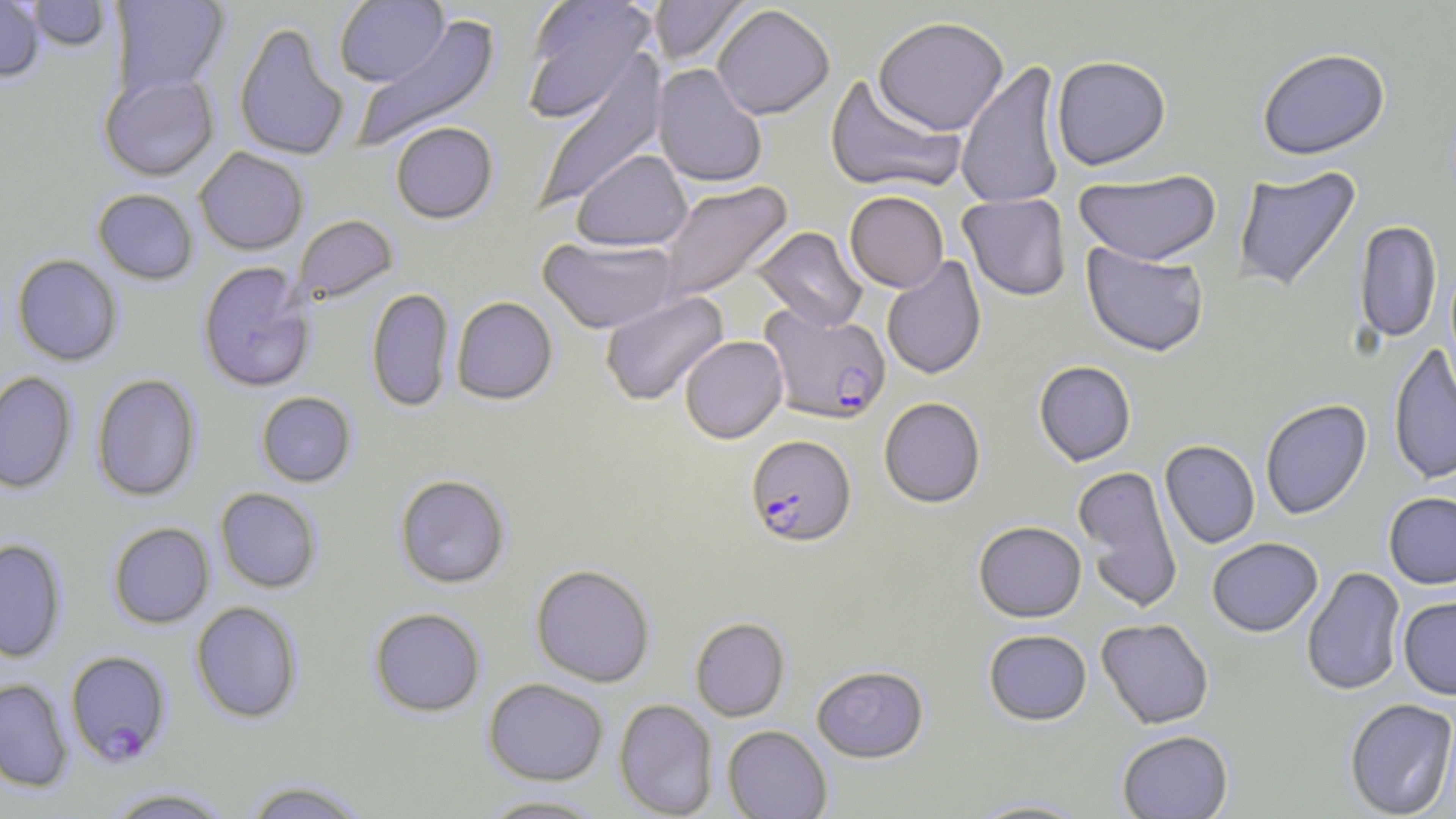
Summary:
  - Coordinate format: approximate bounding boxes as [x1, y1, x2, y2] in pixels
  - Uninfected red blood cell locations: [109, 0, 229, 98], [521, 0, 658, 121], [649, 0, 752, 68], [0, 1, 45, 83], [26, 1, 111, 52], [334, 1, 448, 87], [712, 4, 835, 120], [352, 14, 502, 151], [873, 16, 1009, 135], [234, 20, 349, 162], [1256, 47, 1391, 161], [531, 52, 668, 213], [1051, 55, 1171, 170], [955, 60, 1066, 210], [653, 64, 768, 188], [99, 72, 219, 181], [824, 74, 966, 194], [390, 122, 499, 224], [194, 147, 309, 255], [572, 149, 692, 251], [1232, 165, 1362, 295], [1073, 169, 1221, 266], [655, 180, 794, 305], [92, 188, 198, 285], [844, 190, 949, 292], [958, 193, 1071, 301], [293, 215, 398, 305], [1354, 220, 1442, 343], [751, 226, 869, 332], [538, 236, 680, 333], [1081, 242, 1209, 357], [11, 254, 123, 366], [881, 256, 986, 380], [198, 261, 315, 392], [366, 287, 454, 413], [599, 291, 729, 407], [451, 296, 558, 405], [679, 335, 788, 443], [1388, 342, 1456, 486], [1034, 360, 1137, 466], [0, 371, 77, 494], [91, 373, 201, 502], [256, 391, 356, 487], [879, 396, 986, 508], [1259, 398, 1372, 519], [1160, 440, 1260, 549], [1073, 465, 1183, 612], [395, 474, 510, 588], [215, 487, 322, 593], [1384, 492, 1456, 589], [973, 520, 1086, 622], [108, 522, 215, 629], [1207, 537, 1323, 636], [0, 538, 67, 662], [530, 563, 656, 687], [1301, 566, 1406, 697], [1398, 596, 1456, 699], [190, 601, 303, 724], [369, 607, 486, 717], [690, 617, 790, 721], [1096, 618, 1214, 729], [983, 629, 1092, 725], [811, 665, 929, 762], [483, 677, 608, 785], [0, 678, 73, 792], [614, 698, 718, 819], [1344, 698, 1456, 818], [722, 725, 833, 818], [1117, 730, 1233, 818], [239, 778, 371, 819], [102, 786, 233, 818], [474, 794, 612, 818], [963, 796, 1096, 818]
  - Plasmodium falciparum-infected red blood cell locations: [759, 304, 891, 424], [745, 434, 856, 547], [65, 649, 171, 766]
  - Slide-level diagnosis: Plasmodium falciparum
  - Field of view: single
  - Modality: optical microscopy
  - Stain: May-Grünwald-Giemsa
  - Preparation: thin blood smear
  - Image size: 1456×819 pixels
  - Magnification: 1000x